Describe the morphology of the red blood cells.
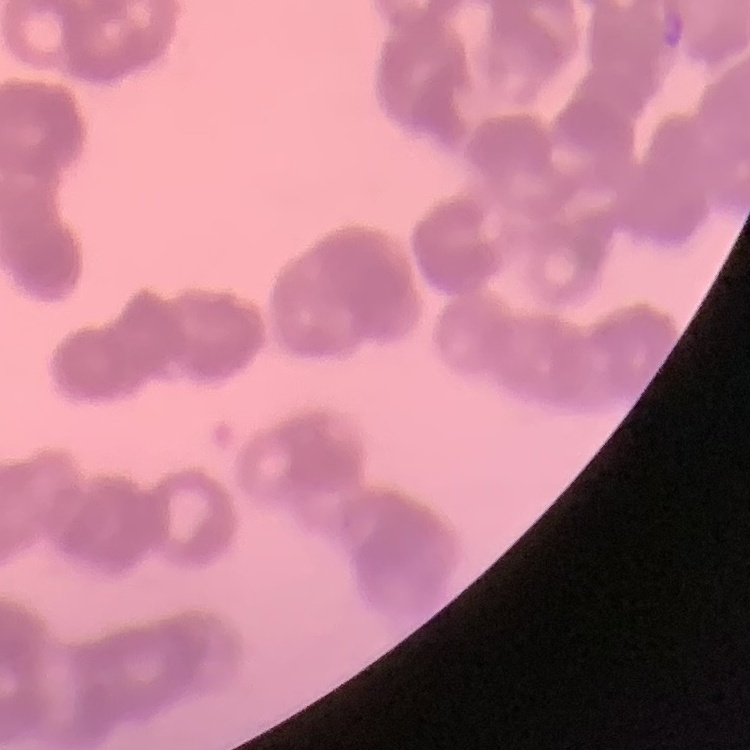

They show rouleaux formation.

{
  "image_type": "square crop of a larger photomicrograph",
  "preparation": "thin peripheral smear",
  "stain": "Field's or Giemsa"
}